Classify this cell by malaria status.
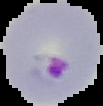
Parasitized.

preparation = thin blood smear
image size = 103×106 pixels
image type = segmented cell region on a black background